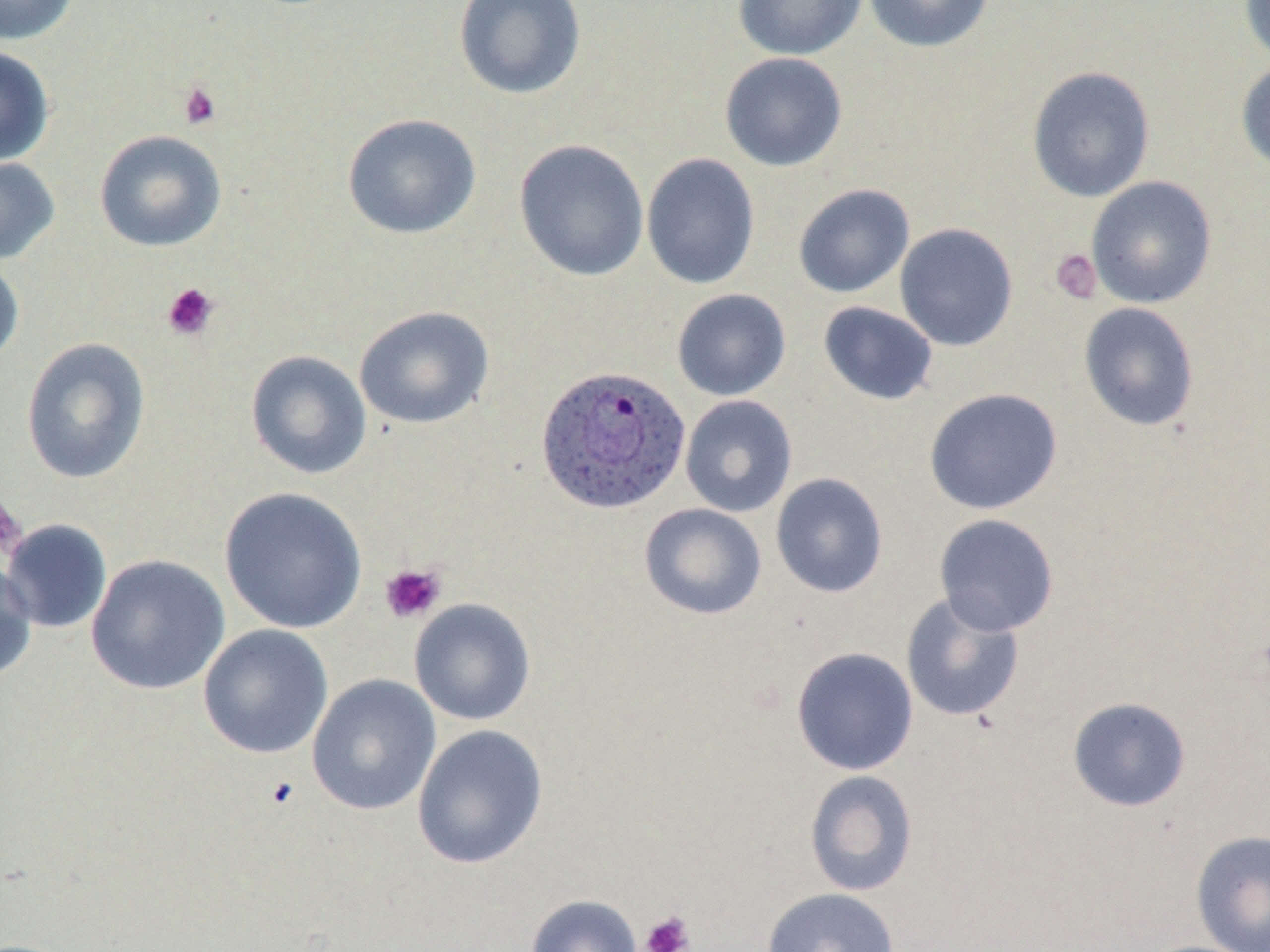 Approximate bounding boxes as [x1, y1, x2, y2] in pixels. Plasmodium ovale-infected red blood cell locations: [534, 364, 690, 515]. Platelet locations: [177, 81, 222, 130], [1049, 248, 1102, 305], [162, 282, 220, 341], [0, 495, 27, 560], [380, 563, 445, 623], [263, 775, 300, 811], [640, 910, 694, 952]. Uninfected red blood cell locations: [0, 0, 80, 45], [452, 0, 587, 100], [732, 0, 868, 60], [862, 0, 995, 53], [1239, 1, 1270, 65], [0, 46, 55, 167], [719, 52, 848, 172], [1235, 58, 1270, 176], [1027, 66, 1156, 203], [342, 113, 482, 239], [94, 129, 227, 252], [514, 139, 649, 282], [641, 152, 760, 289], [0, 156, 60, 265], [1086, 176, 1217, 309], [792, 183, 915, 298], [894, 222, 1018, 351], [0, 254, 24, 368], [671, 289, 791, 401], [818, 301, 939, 406], [1078, 302, 1200, 432], [354, 305, 494, 429], [21, 337, 151, 485], [245, 350, 371, 479], [923, 387, 1063, 515], [679, 394, 797, 517], [770, 472, 889, 598], [219, 486, 367, 634], [639, 503, 767, 620], [933, 513, 1059, 636], [1, 519, 112, 633], [86, 554, 230, 695], [0, 556, 37, 683], [900, 593, 1025, 724], [409, 598, 536, 725], [198, 624, 334, 759], [791, 646, 919, 775], [306, 674, 441, 816], [1067, 696, 1192, 812], [412, 724, 548, 869], [804, 770, 918, 896], [1190, 830, 1270, 952], [761, 887, 900, 952], [525, 894, 642, 952]. Slide-level diagnosis: Plasmodium ovale. Thin blood film. Light microscopy. Image is 1270×952 pixels. 1000x magnification. May-Grünwald-Giemsa-stained preparation. Single field of view.